Name the parasite shown.
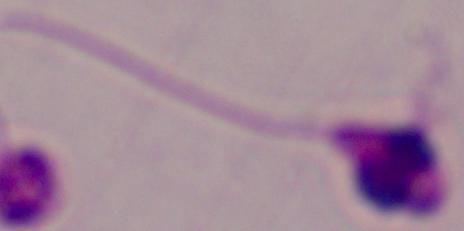

Leishmania.

modality = micrograph
magnification = 1000x